Locate every blood parasite and identify its species.
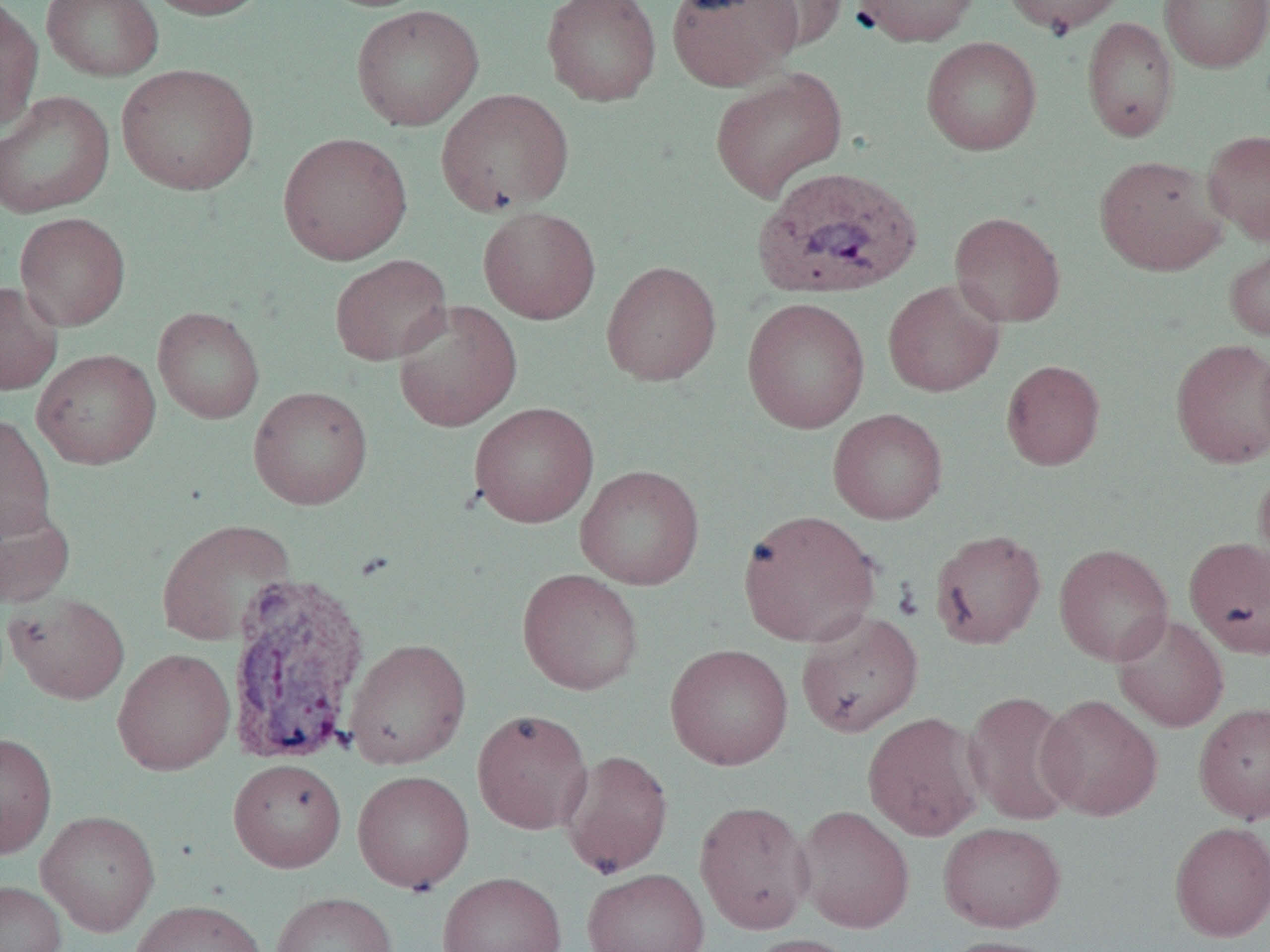
Approximate bounding boxes as [x1, y1, x2, y2] in pixels.
Plasmodium vivax-infected red blood cells: [751, 165, 924, 300], [223, 571, 373, 764].
No Plasmodium falciparum, Plasmodium ovale, Plasmodium malariae, Babesia divergens, or Trypanosoma brucei observed.

Summary:
  - Uninfected red blood cell locations: [42, 0, 164, 81], [142, 0, 270, 20], [541, 0, 662, 106], [666, 0, 803, 91], [852, 0, 980, 47], [1001, 0, 1129, 36], [1159, 0, 1270, 72], [742, 1, 849, 52], [0, 2, 44, 132], [350, 3, 484, 131], [1081, 17, 1179, 142], [921, 37, 1042, 155], [116, 63, 259, 196], [709, 68, 847, 202], [436, 88, 574, 216], [0, 90, 115, 219], [1202, 129, 1270, 244], [278, 132, 412, 265], [1095, 155, 1227, 276], [477, 206, 601, 324], [949, 211, 1065, 327], [14, 212, 130, 331], [1224, 242, 1270, 341], [329, 254, 452, 365], [601, 260, 722, 386], [883, 279, 1005, 397], [0, 282, 63, 395], [741, 297, 871, 433], [392, 299, 523, 432], [153, 307, 265, 424], [1170, 337, 1270, 468], [32, 348, 161, 470], [1001, 359, 1105, 470], [248, 386, 373, 510], [469, 402, 599, 528], [828, 409, 948, 525], [0, 414, 57, 541], [1253, 462, 1270, 590], [574, 464, 705, 589], [0, 497, 75, 609], [738, 509, 881, 647], [156, 518, 295, 647], [930, 529, 1047, 649], [1183, 536, 1270, 657], [1054, 543, 1173, 666], [517, 568, 644, 695], [4, 591, 130, 704], [795, 611, 924, 738], [1112, 613, 1230, 732], [344, 638, 472, 770], [665, 644, 794, 770], [112, 648, 235, 776], [963, 690, 1080, 825], [1036, 694, 1163, 821], [1194, 701, 1270, 825], [472, 708, 593, 835], [862, 711, 987, 842], [0, 732, 57, 859], [559, 749, 673, 878], [228, 758, 347, 872], [352, 770, 474, 893], [694, 799, 814, 934], [794, 804, 915, 933], [36, 810, 160, 936], [938, 821, 1066, 932], [1169, 821, 1270, 942], [582, 868, 710, 952], [437, 871, 568, 952], [0, 880, 66, 952], [270, 890, 397, 952], [130, 899, 269, 952], [743, 934, 859, 952], [937, 936, 1065, 952]
  - Slide-level diagnosis: Plasmodium vivax
  - Modality: light microscopy
  - Image size: 1270×952 pixels
  - Field of view: one of a larger specimen
  - Magnification: 1000x
  - Preparation: thin blood film